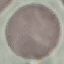

Result: no malaria parasites detected. Giemsa stain. Thin blood film. Acquired by smartphone through the microscope eyepiece. Automatically extracted cell patch, resized to 64 × 64 pixels.